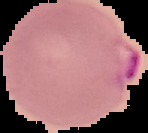
{
  "preparation": "thin blood film",
  "image_size": "148×133 pixels",
  "result": "Plasmodium parasites identified",
  "image_type": "cell region segmented out of the field of view; surrounding area masked to black"
}